Classify the preparation.
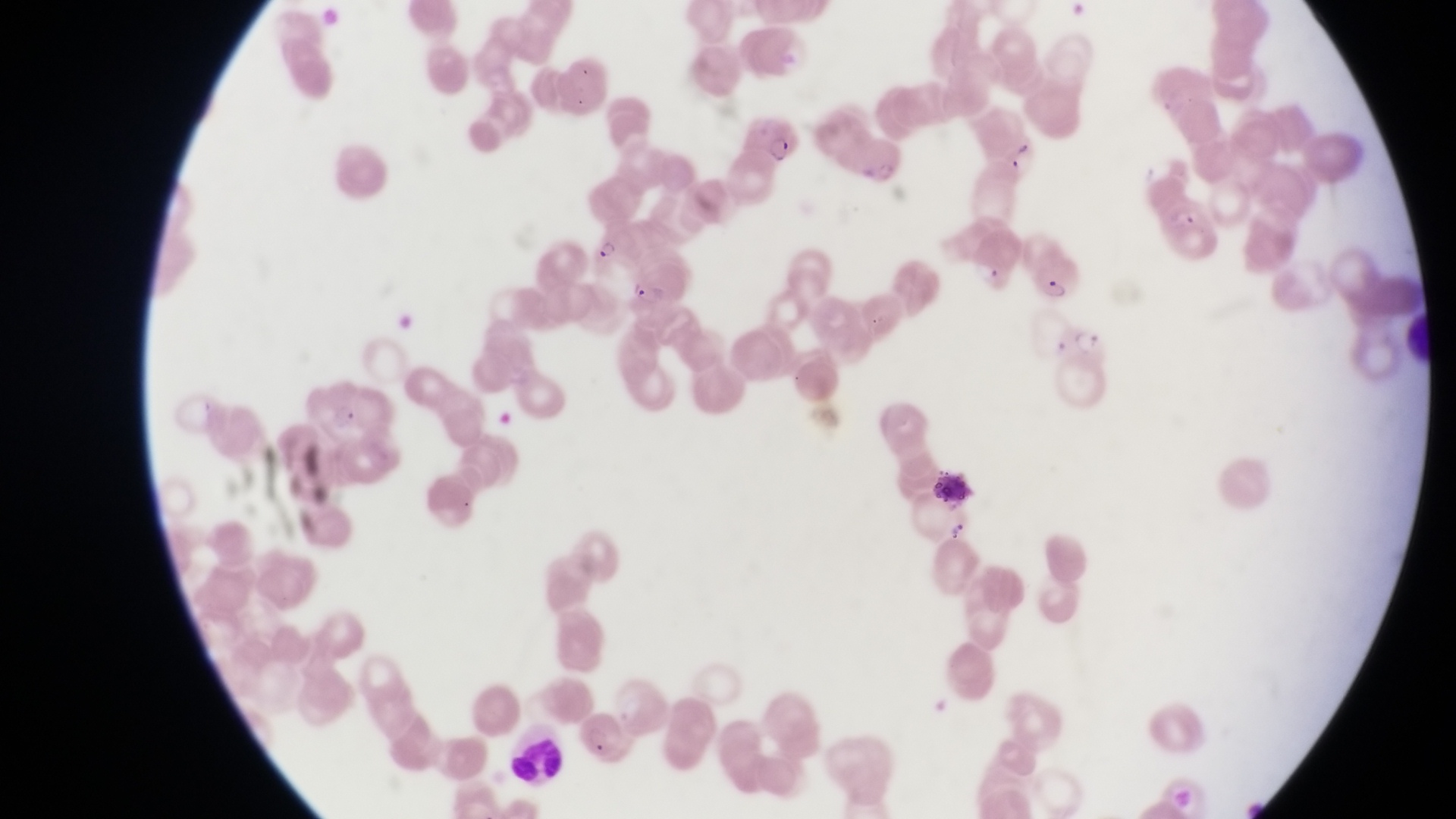
Thin blood smear.

Approximate bounding boxes as left top right bottom in pixels. Artifact (platelet-like body, stain precipitate, or debris) locations: 1004 142 1038 169; 925 468 977 505; 943 518 975 550. Trophozoite locations: 581 228 617 262; 623 281 668 310. Leukocyte locations: 502 742 566 787. Parasitised red blood cell locations: 748 113 801 165; 1052 307 1111 384; 570 710 629 762. At a magnification of 1000x. Sample from Uganda. One field of view. Image is 1456×819 pixels. Captured by a smartphone held over the eyepiece of an Olympus CX-23 microscope.